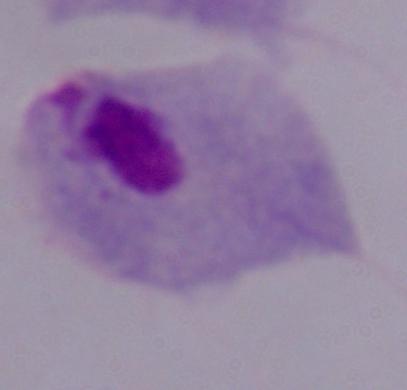
Summary:
  - Modality: micrograph
  - Magnification: 1000x
  - Identification: trichomonad